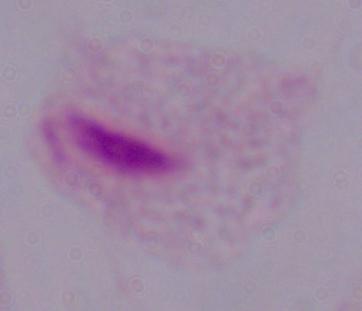
Summary:
  - Identification: trichomonad
  - Magnification: 1000x
  - Modality: micrograph